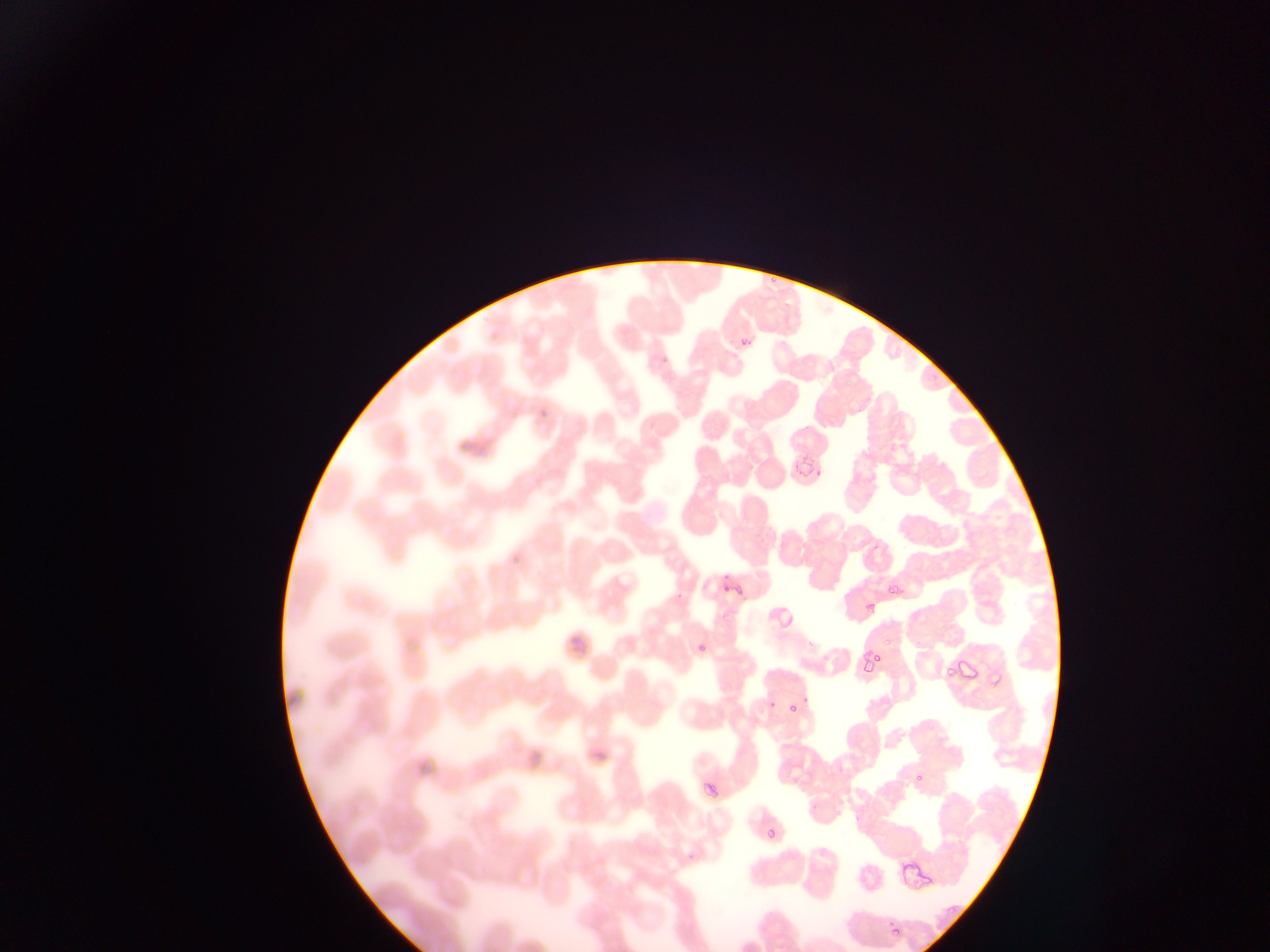

image size = 1270×952 pixels
capture = mobile-phone photograph through a microscope
field of view = single
country = Ghana
preparation = thin blood film
malaria parasite locations = approximate bounding boxes as (left, top, right, bottom) in pixels: (739, 332, 757, 344), (802, 462, 818, 475), (720, 577, 740, 596), (888, 583, 900, 597), (694, 638, 708, 653), (852, 651, 871, 675), (872, 655, 886, 662), (943, 665, 956, 681), (785, 698, 799, 713), (763, 826, 780, 839), (897, 856, 937, 894)